Report the malaria status of this cell.
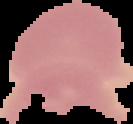

It is uninfected.

Summary:
  - Image size: 133×124 pixels
  - Image type: segmented cell region with the area outside set to black
  - Preparation: thin blood smear